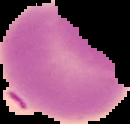

Malaria status: uninfected. Cell region segmented out of the field of view; the surrounding area is masked to black. From a thin blood smear. Image is 130×124 pixels.